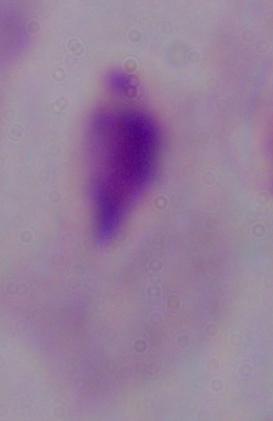 A trichomonad is shown. Photomicrograph. 1000x magnification.